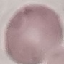
result = negative for malaria parasites
preparation = thin blood smear
image type = automatically extracted cell patch, resized to 64 × 64 pixels
capture = smartphone camera at the microscope eyepiece
stain = Giemsa